Mark where platelets are.
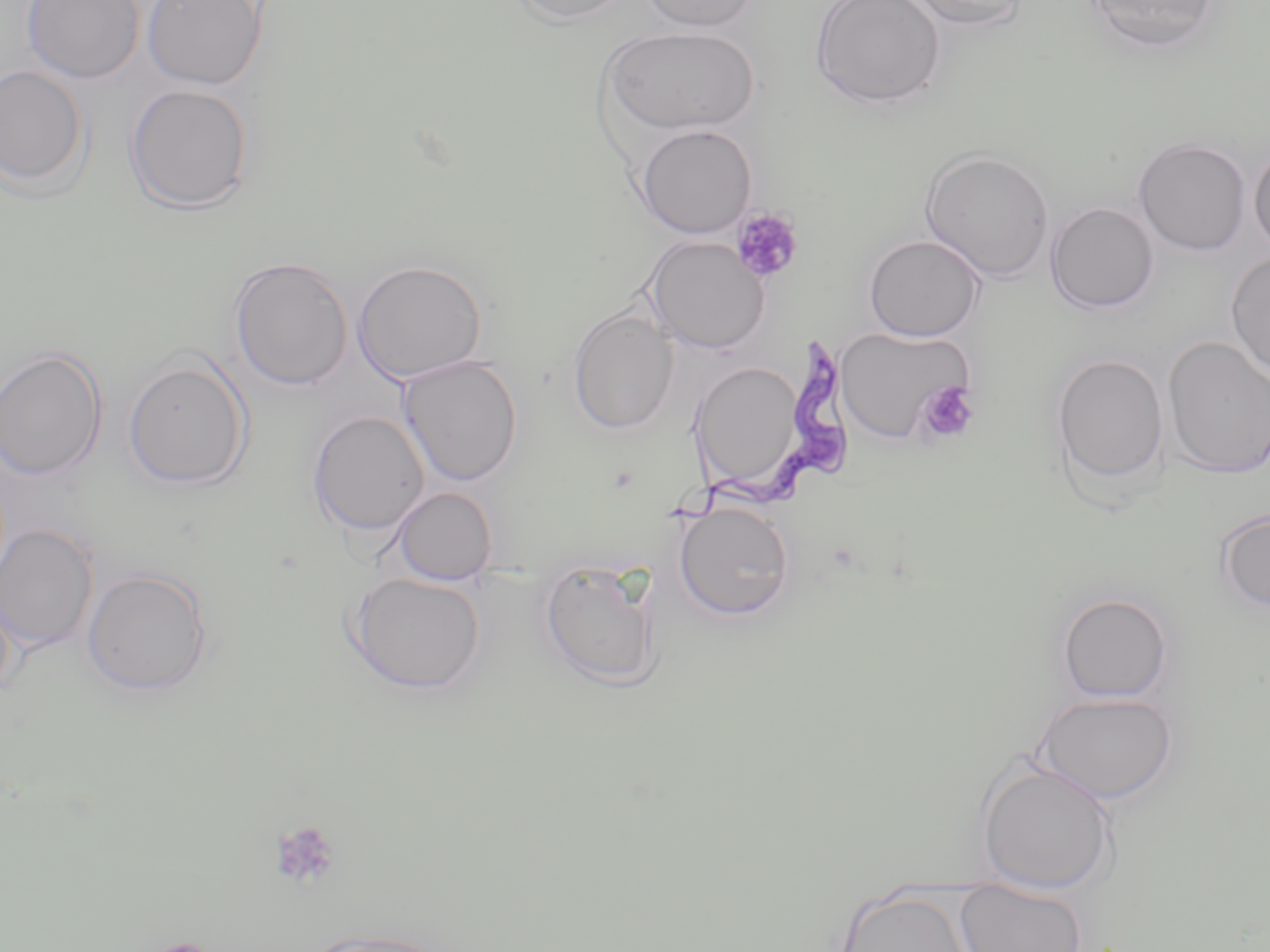
Approximate bounding boxes as [x1, y1, x2, y2] in pixels.
Platelets: [730, 207, 804, 284], [917, 381, 980, 445], [269, 820, 342, 890].

Summary:
  - Uninfected red blood cell locations: [22, 0, 144, 84], [141, 0, 267, 90], [509, 0, 636, 26], [639, 0, 760, 33], [810, 0, 946, 110], [902, 0, 1032, 31], [1083, 0, 1222, 55], [601, 26, 759, 136], [0, 63, 90, 194], [124, 83, 255, 215], [635, 124, 757, 239], [1133, 137, 1252, 256], [1248, 142, 1270, 257], [920, 148, 1056, 282], [1045, 202, 1160, 313], [863, 234, 986, 341], [643, 235, 770, 354], [1226, 252, 1270, 380], [228, 256, 354, 391], [352, 260, 487, 384], [567, 307, 679, 434], [834, 326, 978, 444], [1162, 337, 1270, 478], [0, 347, 107, 481], [1049, 352, 1170, 497], [397, 355, 523, 487], [123, 356, 252, 491], [689, 359, 808, 493], [306, 410, 431, 537], [391, 487, 498, 585], [673, 500, 796, 621], [1216, 509, 1270, 613], [0, 524, 99, 651], [539, 560, 661, 688], [82, 566, 215, 698], [347, 571, 487, 695], [0, 586, 15, 702], [1056, 592, 1174, 703], [1035, 691, 1179, 804], [974, 756, 1118, 894], [954, 882, 1089, 952], [834, 886, 974, 952], [296, 927, 454, 952]
  - Trypanosoma brucei locations: [661, 336, 844, 527]
  - Slide-level diagnosis: Trypanosoma brucei
  - Magnification: 1000x
  - Field of view: one of a larger specimen
  - Image size: 1270×952 pixels
  - Modality: light microscopy
  - Stain: May-Grünwald-Giemsa
  - Preparation: thin blood film